Classify the preparation.
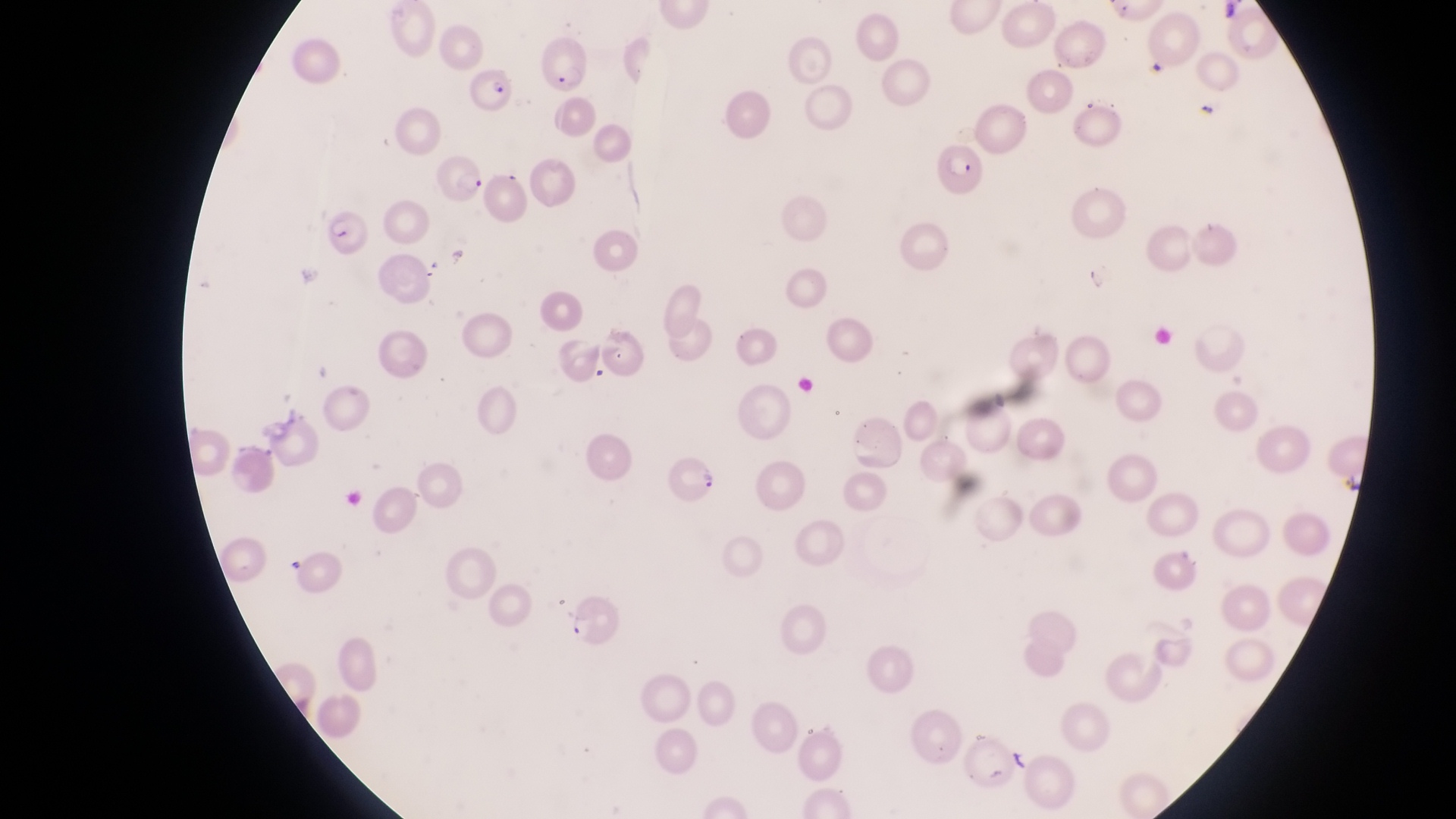
Thin blood film.

Approximate bounding boxes as (left, top, right, bottom) in pixels.
Summary:
  - Trophozoite locations: (444, 240, 474, 272)
  - Parasitised red blood cell locations: (535, 36, 590, 95), (465, 64, 518, 114), (934, 138, 984, 194), (436, 158, 488, 207), (323, 212, 370, 257), (597, 320, 647, 379), (670, 452, 725, 507), (1152, 536, 1204, 599), (560, 591, 619, 650)
  - Artifact (platelet-like body, stain precipitate, or debris) locations: (1198, 98, 1217, 122), (1012, 746, 1031, 776)
  - Magnification: 1000x
  - Capture: smartphone photograph through the eyepiece of an Olympus CX-23 microscope
  - Field of view: single
  - Country: Uganda
  - Image size: 1456×819 pixels